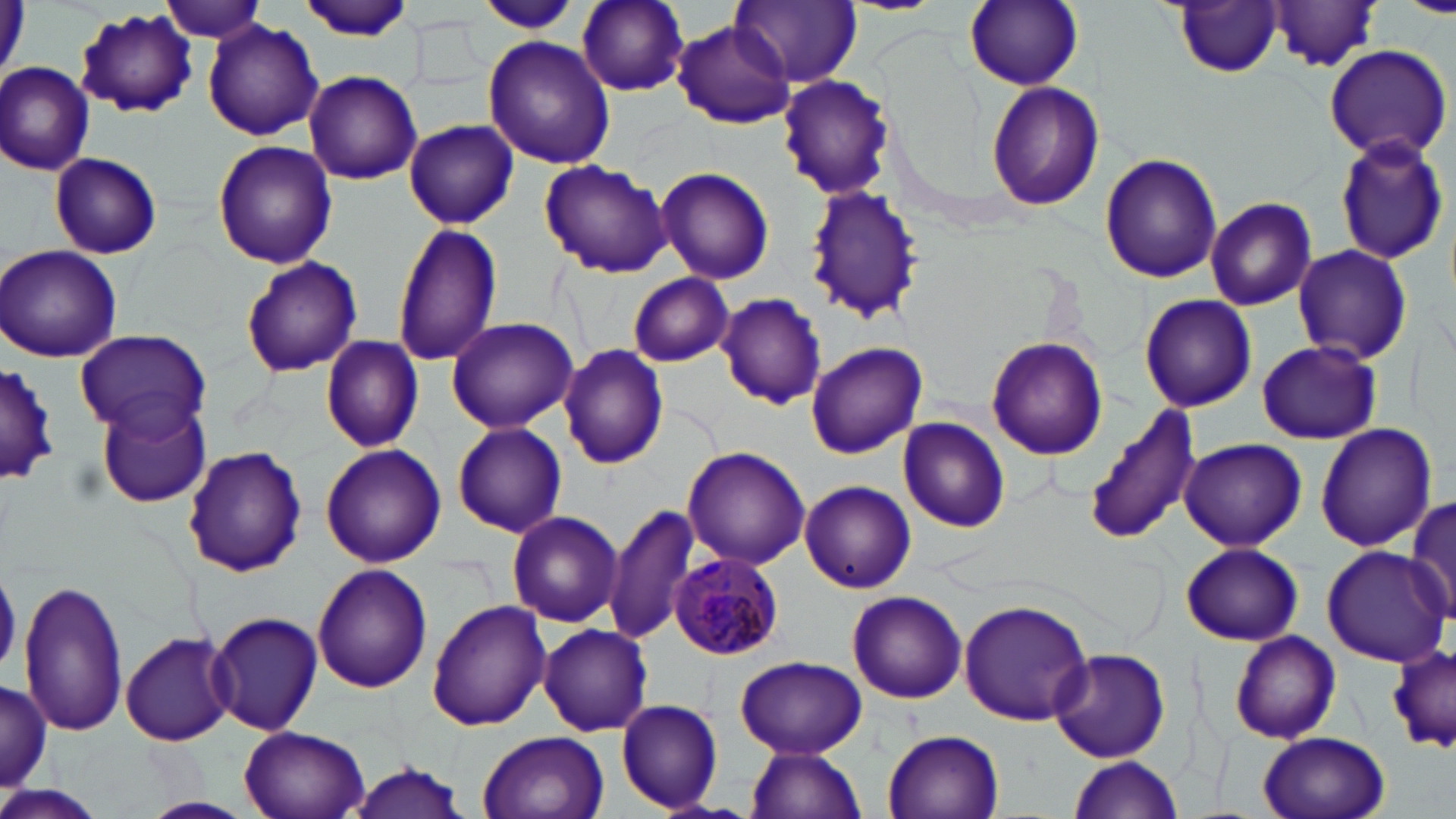 Approximate bounding boxes as (x1,y1)-(x2,y2) corner pairs in pixels. Plasmodium malariae-infected red blood cell locations: (671,551)-(784,660). Uninfected red blood cell locations: (577,0)-(690,95), (731,0)-(861,87), (964,0)-(1083,90), (1402,0)-(1456,19), (159,1)-(267,43), (298,1)-(415,42), (1171,2)-(1285,78), (475,3)-(583,35), (1264,3)-(1387,72), (73,6)-(198,119), (671,20)-(795,129), (203,21)-(324,140), (483,36)-(617,171), (1323,44)-(1452,162), (1,62)-(95,175), (304,70)-(421,183), (776,74)-(896,200), (987,80)-(1103,209), (405,119)-(518,229), (1332,134)-(1449,267), (213,139)-(337,270), (50,151)-(162,260), (1099,151)-(1222,284), (538,159)-(671,278), (656,167)-(775,284), (801,186)-(925,328), (1205,197)-(1317,310), (390,224)-(505,367), (1,243)-(124,361), (1291,243)-(1414,365), (240,255)-(363,377), (627,273)-(734,365), (716,293)-(827,410), (1138,293)-(1257,412), (445,315)-(579,433), (76,329)-(212,441), (986,335)-(1106,460), (321,336)-(426,453), (1256,340)-(1380,445), (807,342)-(926,459), (558,344)-(669,469), (0,360)-(62,488), (94,397)-(213,510), (1083,404)-(1203,547), (897,415)-(1011,532), (451,422)-(568,538), (1316,424)-(1437,552), (1179,437)-(1307,551), (320,443)-(446,568), (183,445)-(308,577), (682,446)-(811,570), (800,480)-(916,593), (1408,499)-(1456,619), (605,501)-(702,647), (506,509)-(624,628), (1182,541)-(1304,647), (1321,544)-(1452,667), (311,563)-(432,692), (17,574)-(131,740), (847,590)-(967,704), (958,597)-(1097,724), (427,601)-(551,732), (209,610)-(325,735), (536,624)-(654,737), (121,631)-(233,746), (1229,632)-(1341,744), (1387,643)-(1456,752), (1050,647)-(1172,763), (735,655)-(868,759), (1,676)-(50,794), (615,699)-(724,813), (238,725)-(371,819), (883,730)-(1005,818), (478,731)-(609,819), (1257,732)-(1390,819), (746,746)-(866,819), (1068,755)-(1184,818), (349,757)-(465,819), (0,781)-(108,819), (139,795)-(254,819). Slide-level diagnosis: Plasmodium malariae. May-Grünwald-Giemsa stain. Thin blood film. One field of a larger specimen. Optical microscopy. Image is 1456×819 pixels. Captured at 1000x magnification.